Classify this cell by malaria status.
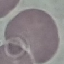

Uninfected.

Photographed with a smartphone camera at the microscope eyepiece. Thin blood film. Giemsa-stained preparation. Cell patch, automatically extracted from a larger field of view and resized to 64 × 64 pixels.